Assess this cell for malaria.
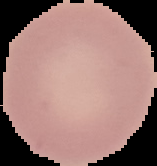

It is uninfected.

Summary:
  - Image size: 157×166 pixels
  - Preparation: thin blood smear
  - Image type: segmented cell region with the area outside set to black